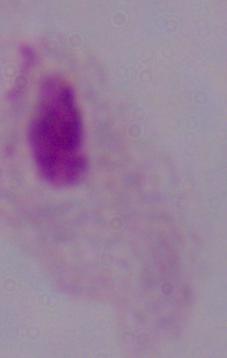

Summary:
  - Identification: trichomonad
  - Modality: micrograph
  - Magnification: 1000x